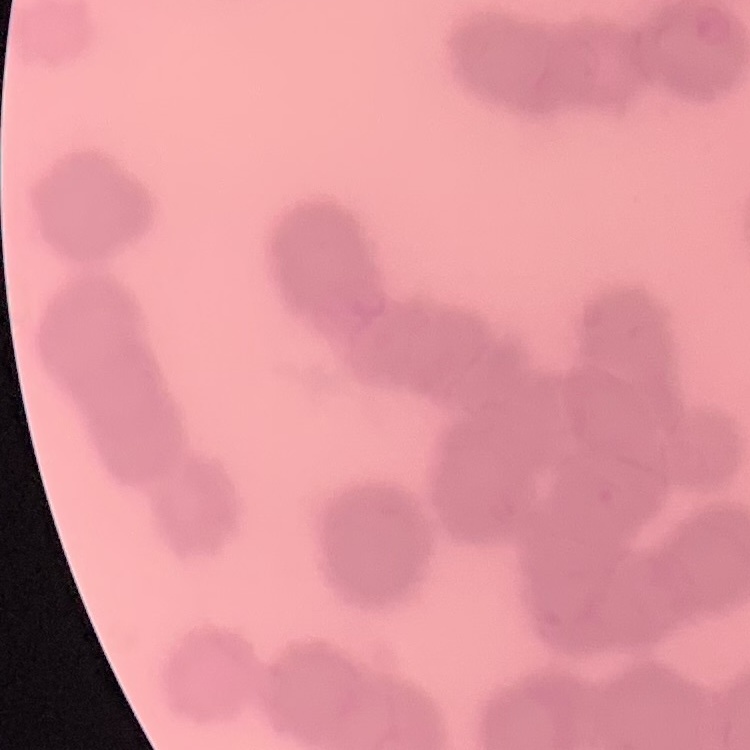

Summary:
  - Red blood cell morphology: rouleaux formation
  - Image type: square crop of a larger photomicrograph
  - Stain: Field's or Giemsa
  - Preparation: thin peripheral smear